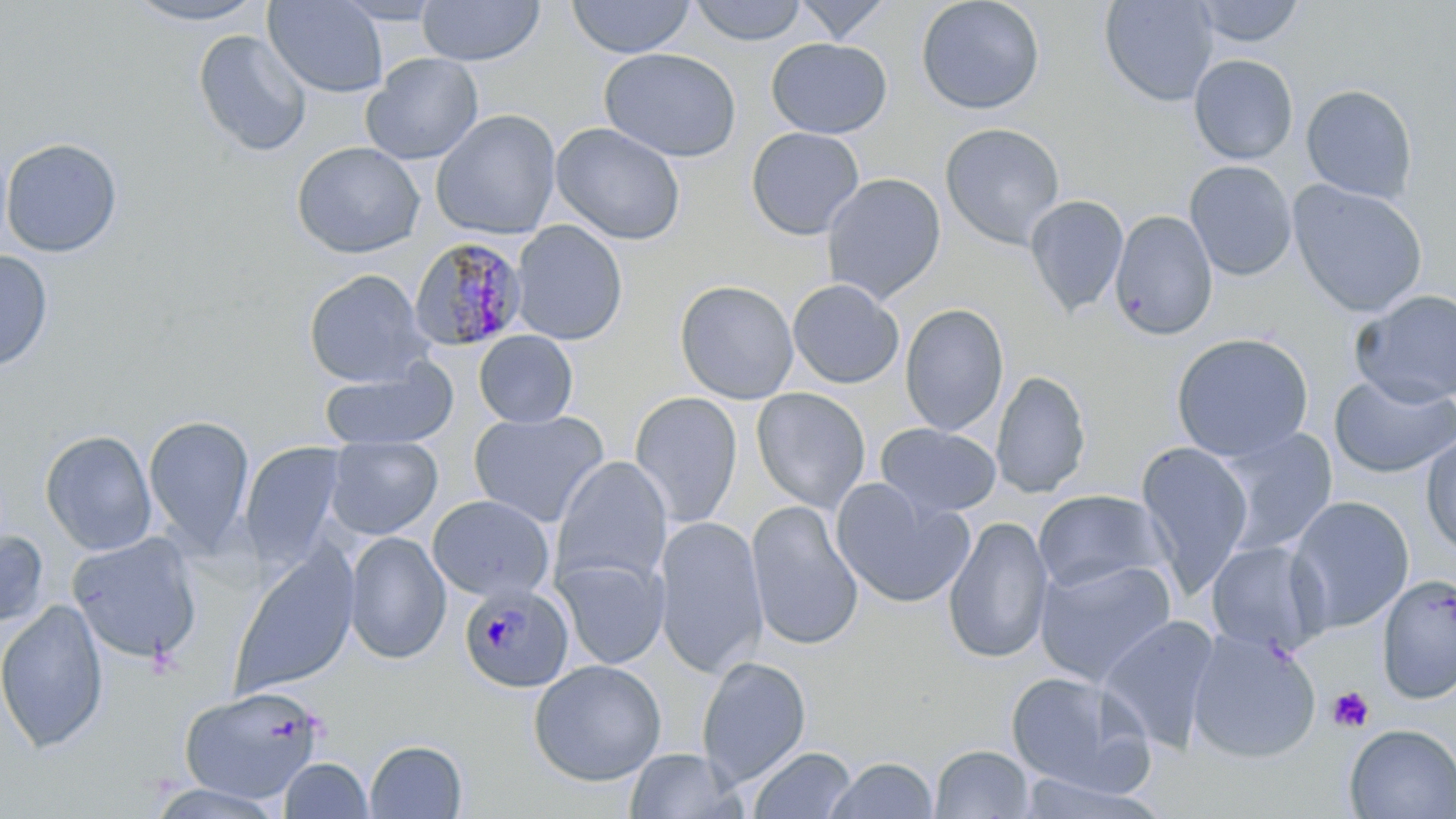
slide-level diagnosis = Plasmodium malariae
magnification = 1000x
platelet locations = approximate bounding boxes as named x1/y1/x2/y2 corners in pixels: (x1=1328, y1=687, x2=1374, y2=733)
uninfected red blood cell locations = approximate bounding boxes as named x1/y1/x2/y2 corners in pixels: (x1=124, y1=0, x2=269, y2=26), (x1=330, y1=0, x2=447, y2=25), (x1=566, y1=0, x2=696, y2=59), (x1=689, y1=0, x2=808, y2=46), (x1=793, y1=0, x2=896, y2=43), (x1=915, y1=0, x2=1046, y2=115), (x1=1099, y1=0, x2=1218, y2=106), (x1=1191, y1=0, x2=1307, y2=48), (x1=263, y1=1, x2=389, y2=98), (x1=416, y1=1, x2=545, y2=66), (x1=192, y1=29, x2=312, y2=158), (x1=766, y1=37, x2=892, y2=139), (x1=599, y1=47, x2=741, y2=162), (x1=361, y1=53, x2=484, y2=165), (x1=1188, y1=54, x2=1299, y2=164), (x1=1300, y1=83, x2=1418, y2=205), (x1=431, y1=110, x2=561, y2=239), (x1=551, y1=122, x2=687, y2=245), (x1=940, y1=122, x2=1066, y2=249), (x1=745, y1=127, x2=865, y2=241), (x1=0, y1=137, x2=122, y2=258), (x1=291, y1=141, x2=425, y2=259), (x1=1185, y1=160, x2=1297, y2=281), (x1=821, y1=173, x2=946, y2=304), (x1=1289, y1=180, x2=1428, y2=318), (x1=1024, y1=194, x2=1129, y2=317), (x1=1109, y1=210, x2=1218, y2=341), (x1=511, y1=221, x2=628, y2=346), (x1=0, y1=249, x2=54, y2=372), (x1=303, y1=269, x2=432, y2=387), (x1=787, y1=278, x2=904, y2=389), (x1=674, y1=279, x2=799, y2=404), (x1=1352, y1=290, x2=1456, y2=407), (x1=899, y1=303, x2=1009, y2=437), (x1=474, y1=330, x2=578, y2=428), (x1=1171, y1=332, x2=1314, y2=462), (x1=319, y1=361, x2=458, y2=452), (x1=991, y1=370, x2=1091, y2=499), (x1=1329, y1=373, x2=1456, y2=478), (x1=751, y1=387, x2=871, y2=513), (x1=629, y1=391, x2=743, y2=529), (x1=468, y1=410, x2=609, y2=528), (x1=142, y1=413, x2=255, y2=555), (x1=875, y1=423, x2=1002, y2=519), (x1=1214, y1=427, x2=1339, y2=557), (x1=39, y1=429, x2=157, y2=556), (x1=1419, y1=432, x2=1456, y2=558), (x1=324, y1=435, x2=443, y2=539), (x1=238, y1=442, x2=346, y2=568), (x1=1135, y1=443, x2=1254, y2=597), (x1=551, y1=455, x2=673, y2=592), (x1=830, y1=479, x2=974, y2=609), (x1=1033, y1=489, x2=1170, y2=596), (x1=428, y1=495, x2=555, y2=602), (x1=1285, y1=495, x2=1415, y2=635), (x1=746, y1=500, x2=864, y2=652), (x1=942, y1=515, x2=1054, y2=665), (x1=654, y1=516, x2=768, y2=678), (x1=0, y1=527, x2=49, y2=628), (x1=66, y1=531, x2=204, y2=665), (x1=344, y1=532, x2=451, y2=664), (x1=1206, y1=540, x2=1327, y2=655), (x1=229, y1=543, x2=360, y2=698), (x1=555, y1=556, x2=669, y2=669), (x1=1034, y1=557, x2=1178, y2=687), (x1=1375, y1=573, x2=1456, y2=704), (x1=0, y1=599, x2=109, y2=754), (x1=1097, y1=614, x2=1222, y2=753), (x1=1186, y1=628, x2=1322, y2=764), (x1=696, y1=656, x2=812, y2=787), (x1=528, y1=659, x2=667, y2=786), (x1=1005, y1=671, x2=1153, y2=795), (x1=178, y1=684, x2=326, y2=803), (x1=1343, y1=724, x2=1456, y2=818), (x1=364, y1=739, x2=468, y2=818), (x1=747, y1=745, x2=857, y2=819), (x1=929, y1=745, x2=1036, y2=818), (x1=624, y1=747, x2=746, y2=819), (x1=278, y1=757, x2=373, y2=818), (x1=824, y1=757, x2=938, y2=818), (x1=1014, y1=771, x2=1167, y2=818), (x1=144, y1=783, x2=288, y2=818)
stain = May-Grünwald-Giemsa
image size = 1456×819 pixels
preparation = thin blood smear
Plasmodium malariae-infected red blood cell locations = approximate bounding boxes as named x1/y1/x2/y2 corners in pixels: (x1=408, y1=236, x2=528, y2=353), (x1=459, y1=582, x2=574, y2=692)
field of view = one of a larger specimen
modality = light microscopy